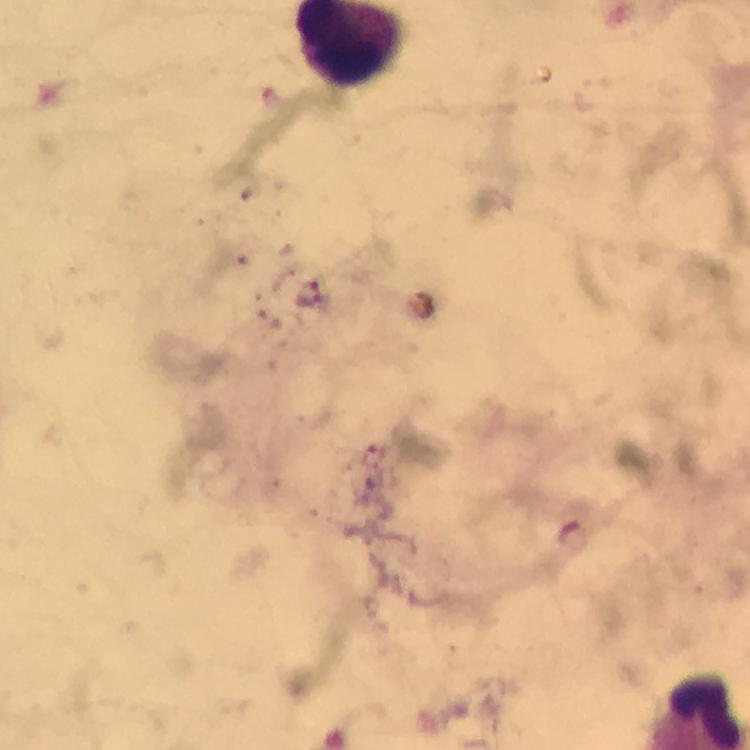
stain = Giemsa
preparation = thick blood film
magnification = 100x
capture = smartphone photograph through a microscope
immersion oil = applied
image size = 750×750 pixels
cropped from = one field of view
context = from a diagnostic examination for malaria
Plasmodium parasite locations = approximate centers as {x, y} in pixels: {308, 302}